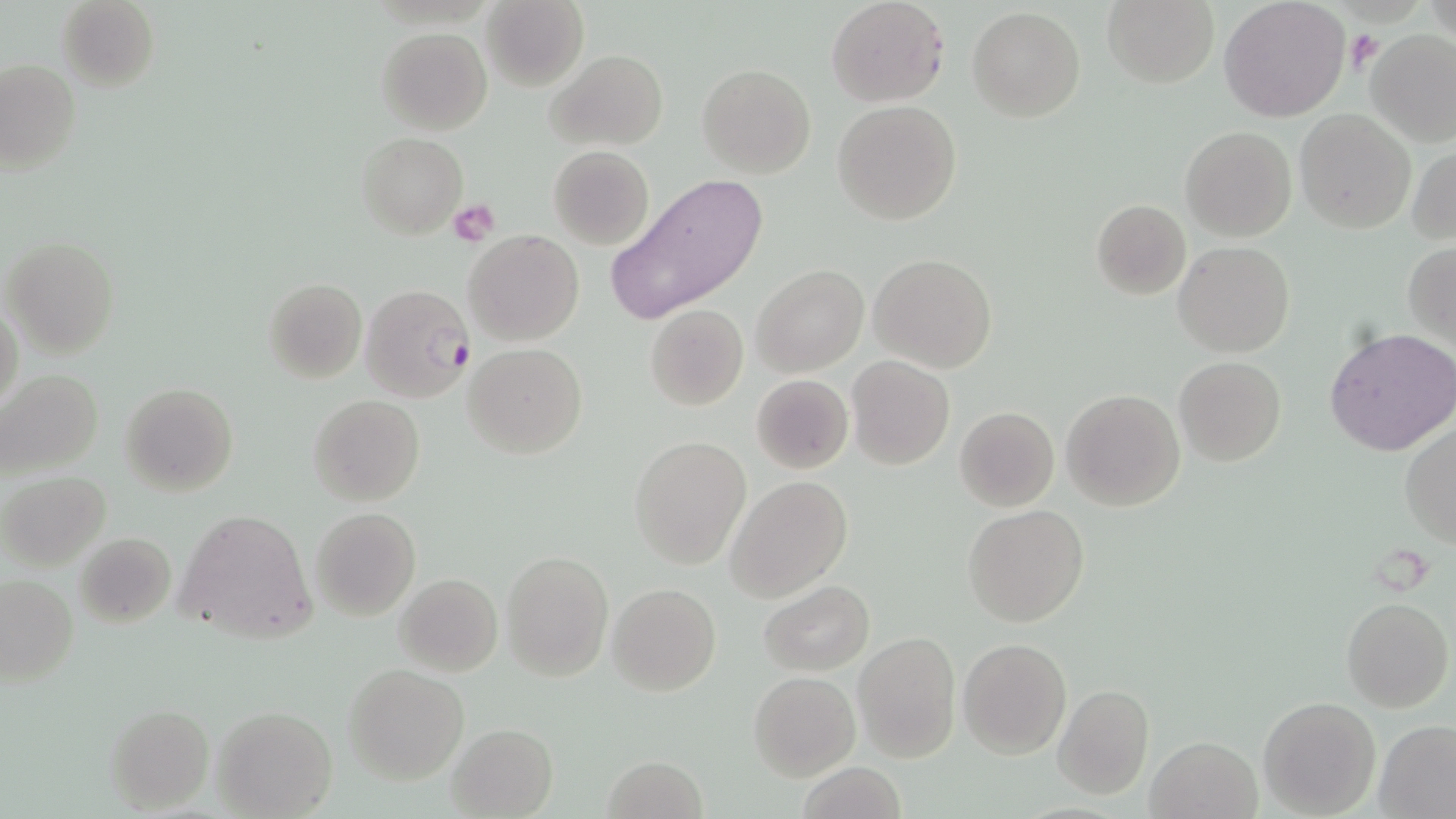

slide-level diagnosis = Plasmodium falciparum
stain = May-Grünwald-Giemsa
platelet locations = approximate bounding boxes as (x1, y1, x2, y2) in pixels: (1345, 28, 1381, 73), (450, 199, 500, 244)
modality = optical microscopy
uninfected red blood cell locations = approximate bounding boxes as (x1, y1, x2, y2) in pixels: (56, 0, 160, 91), (482, 0, 588, 90), (826, 0, 947, 107), (1102, 0, 1218, 88), (1218, 1, 1350, 120), (967, 7, 1086, 124), (376, 27, 492, 133), (1365, 30, 1456, 147), (1341, 38, 1450, 217), (545, 49, 667, 151), (1, 60, 80, 175), (699, 64, 816, 178), (833, 100, 961, 225), (1295, 110, 1416, 233), (1180, 127, 1296, 242), (357, 132, 466, 237), (548, 145, 655, 249), (1408, 145, 1456, 246), (605, 172, 770, 325), (1091, 199, 1192, 300), (465, 229, 583, 346), (4, 238, 119, 358), (1172, 241, 1295, 358), (1403, 241, 1456, 349), (869, 253, 998, 374), (753, 265, 869, 378), (263, 277, 366, 384), (1, 300, 23, 417), (645, 304, 749, 411), (1325, 328, 1456, 458), (466, 343, 586, 459), (1174, 356, 1287, 467), (847, 357, 956, 471), (0, 368, 103, 481), (750, 374, 853, 474), (120, 382, 238, 498), (1061, 389, 1185, 512), (308, 394, 425, 507), (955, 406, 1058, 511), (1400, 424, 1456, 545), (628, 435, 753, 570), (2, 471, 110, 570), (727, 476, 853, 603), (962, 506, 1089, 626), (311, 507, 421, 621), (174, 508, 315, 644), (73, 531, 175, 628), (501, 548, 612, 680), (395, 573, 503, 676), (0, 575, 79, 687), (760, 581, 874, 674), (608, 583, 720, 695), (1341, 597, 1453, 712), (853, 632, 961, 762), (957, 636, 1071, 757), (343, 664, 469, 784), (749, 671, 859, 781), (1054, 685, 1153, 800), (1258, 696, 1381, 818), (105, 704, 213, 811), (213, 706, 337, 818), (1376, 720, 1456, 817), (446, 723, 558, 818), (1146, 734, 1262, 819), (603, 755, 706, 819), (799, 762, 908, 819)
preparation = thin blood smear
field of view = one of a larger specimen
magnification = 1000x
Plasmodium falciparum-infected red blood cell locations = approximate bounding boxes as (x1, y1, x2, y2) in pixels: (359, 283, 474, 402)
image size = 1456×819 pixels